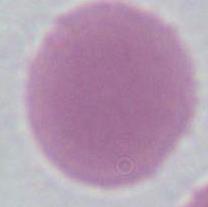

Summary:
  - Magnification: 1000x
  - Modality: micrograph
  - Identification: erythrocyte